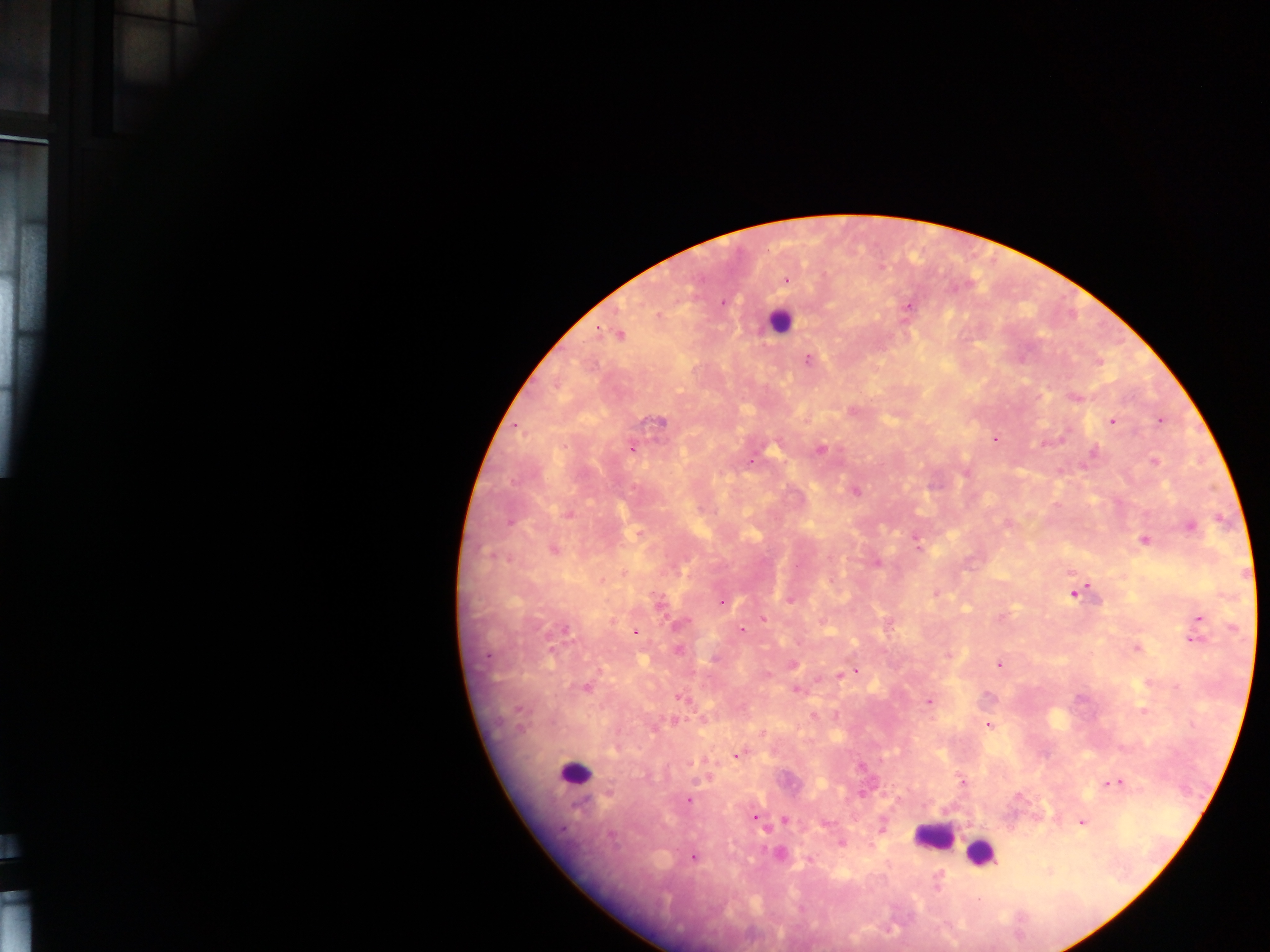

Plasmodium parasite locations = approximate centers as [x, y] in pixels: [786, 279], [723, 303], [907, 308], [620, 334], [808, 359], [1077, 398], [1160, 421], [658, 422], [1112, 422], [995, 438], [632, 449], [821, 450], [1093, 453], [751, 460], [1155, 462], [855, 491], [568, 514], [510, 523], [1007, 524], [1190, 527], [1143, 540], [918, 547], [553, 549], [488, 555], [876, 563], [797, 565], [603, 581], [935, 594], [1075, 594], [789, 601], [723, 602], [659, 603], [1200, 618], [763, 619], [679, 624], [565, 629], [741, 629], [635, 632], [1192, 640], [1137, 649], [678, 650], [552, 651], [487, 656], [715, 659], [999, 664], [792, 665], [855, 672], [768, 674], [840, 675], [586, 688], [796, 690], [680, 698], [929, 701], [519, 709], [812, 715], [988, 725], [520, 728], [738, 755], [690, 762], [860, 767], [962, 781], [1116, 782], [688, 800], [754, 817], [785, 820], [1082, 822], [611, 835], [841, 843], [694, 857], [809, 859], [939, 875], [938, 888], [978, 899]
image size = 1270×952 pixels
country = Ghana
capture = mobile-phone photograph through a microscope
leukocyte locations = approximate centers as [x, y] in pixels: [778, 321], [575, 774], [932, 836], [980, 854]
preparation = thick blood smear
field of view = single